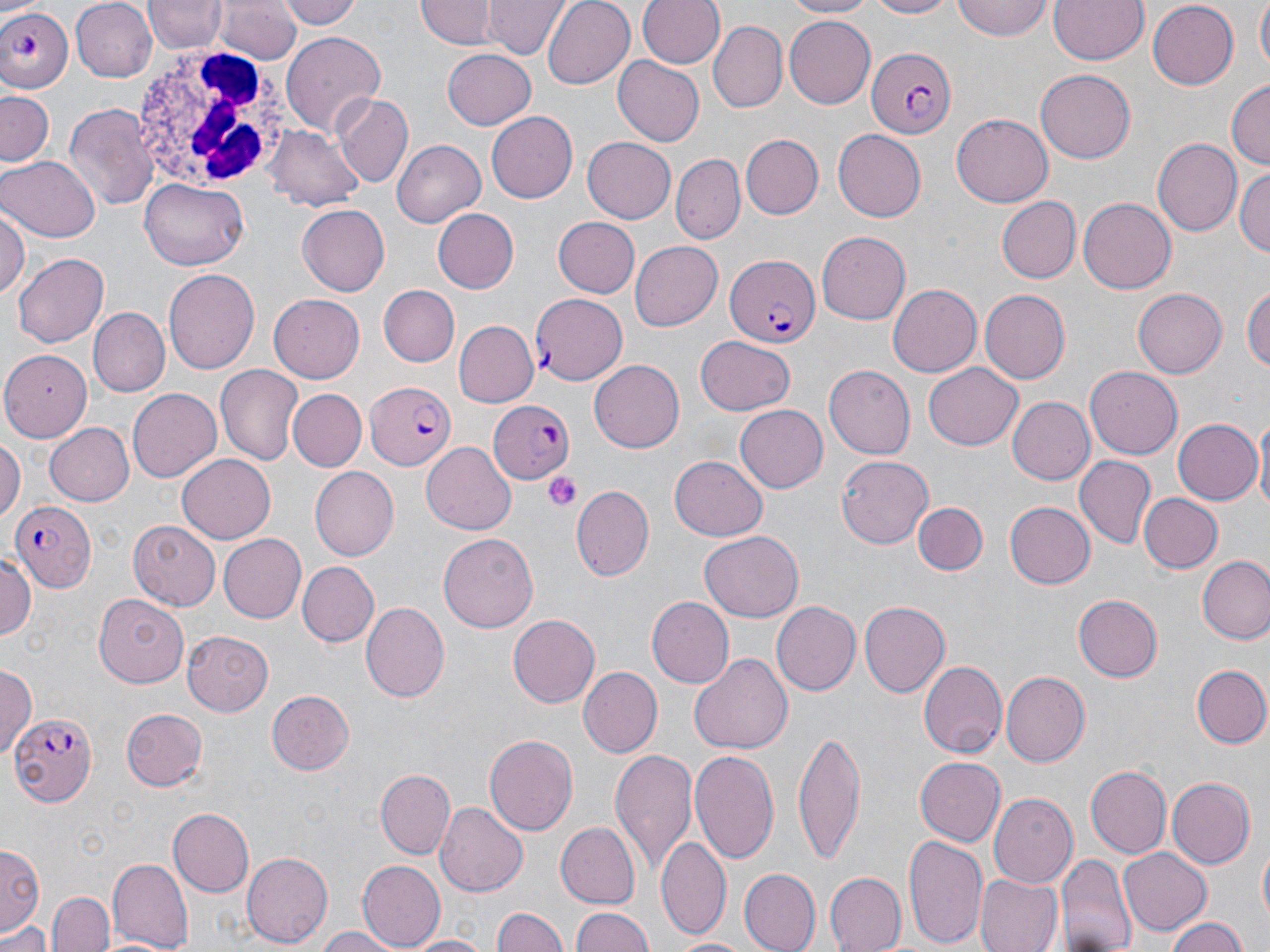

Summary:
  - Coordinate format: approximate bounding boxes as named x1/y1/x2/y2 corners in pixels
  - White blood cell locations: (x1=132, y1=45, x2=301, y2=196)
  - Plasmodium falciparum-infected red blood cell locations: (x1=2, y1=3, x2=75, y2=92), (x1=867, y1=48, x2=956, y2=139), (x1=724, y1=253, x2=817, y2=346), (x1=529, y1=293, x2=629, y2=386), (x1=364, y1=383, x2=453, y2=470), (x1=486, y1=399, x2=575, y2=481), (x1=14, y1=499, x2=96, y2=591), (x1=9, y1=710, x2=96, y2=808)
  - Platelet locations: (x1=543, y1=469, x2=584, y2=511)
  - Uninfected red blood cell locations: (x1=146, y1=0, x2=225, y2=54), (x1=281, y1=0, x2=362, y2=32), (x1=418, y1=0, x2=496, y2=50), (x1=486, y1=0, x2=567, y2=60), (x1=542, y1=0, x2=635, y2=89), (x1=638, y1=0, x2=724, y2=69), (x1=780, y1=0, x2=882, y2=18), (x1=860, y1=0, x2=961, y2=19), (x1=953, y1=0, x2=1052, y2=41), (x1=1049, y1=0, x2=1147, y2=65), (x1=1254, y1=0, x2=1270, y2=71), (x1=73, y1=1, x2=157, y2=82), (x1=217, y1=1, x2=301, y2=65), (x1=1146, y1=3, x2=1240, y2=88), (x1=785, y1=16, x2=875, y2=108), (x1=709, y1=22, x2=786, y2=110), (x1=281, y1=31, x2=386, y2=139), (x1=441, y1=48, x2=537, y2=129), (x1=612, y1=57, x2=704, y2=148), (x1=1036, y1=69, x2=1135, y2=162), (x1=1227, y1=79, x2=1270, y2=173), (x1=1, y1=89, x2=55, y2=167), (x1=334, y1=93, x2=413, y2=187), (x1=63, y1=103, x2=160, y2=211), (x1=485, y1=108, x2=577, y2=200), (x1=951, y1=115, x2=1054, y2=206), (x1=266, y1=126, x2=366, y2=210), (x1=833, y1=128, x2=926, y2=219), (x1=741, y1=134, x2=823, y2=219), (x1=582, y1=136, x2=676, y2=222), (x1=390, y1=138, x2=484, y2=227), (x1=1153, y1=138, x2=1241, y2=238), (x1=672, y1=154, x2=744, y2=241), (x1=0, y1=155, x2=99, y2=242), (x1=1233, y1=167, x2=1269, y2=256), (x1=140, y1=177, x2=251, y2=269), (x1=995, y1=195, x2=1081, y2=283), (x1=1079, y1=196, x2=1177, y2=294), (x1=296, y1=205, x2=390, y2=296), (x1=0, y1=209, x2=29, y2=301), (x1=432, y1=209, x2=519, y2=293), (x1=552, y1=217, x2=639, y2=298), (x1=818, y1=231, x2=910, y2=324), (x1=631, y1=240, x2=723, y2=329), (x1=13, y1=253, x2=109, y2=347), (x1=164, y1=269, x2=260, y2=374), (x1=1243, y1=282, x2=1270, y2=379), (x1=377, y1=284, x2=460, y2=366), (x1=886, y1=285, x2=980, y2=378), (x1=1133, y1=286, x2=1227, y2=375), (x1=978, y1=290, x2=1069, y2=384), (x1=268, y1=294, x2=365, y2=383), (x1=90, y1=308, x2=168, y2=396), (x1=453, y1=321, x2=539, y2=408), (x1=697, y1=334, x2=795, y2=415), (x1=0, y1=350, x2=92, y2=441), (x1=590, y1=359, x2=689, y2=452), (x1=924, y1=362, x2=1024, y2=450), (x1=1086, y1=364, x2=1183, y2=456), (x1=215, y1=365, x2=303, y2=465), (x1=824, y1=365, x2=915, y2=459), (x1=126, y1=388, x2=219, y2=482), (x1=287, y1=388, x2=366, y2=471), (x1=1006, y1=396, x2=1095, y2=485), (x1=737, y1=407, x2=827, y2=491), (x1=1254, y1=417, x2=1270, y2=518), (x1=1171, y1=418, x2=1260, y2=505), (x1=45, y1=422, x2=134, y2=506), (x1=0, y1=437, x2=23, y2=524), (x1=421, y1=442, x2=516, y2=535), (x1=177, y1=454, x2=275, y2=542), (x1=834, y1=455, x2=933, y2=548), (x1=1076, y1=455, x2=1154, y2=547), (x1=670, y1=456, x2=769, y2=541), (x1=310, y1=467, x2=400, y2=559), (x1=570, y1=485, x2=654, y2=582), (x1=1138, y1=493, x2=1222, y2=573), (x1=1004, y1=501, x2=1095, y2=589), (x1=912, y1=502, x2=988, y2=576), (x1=131, y1=519, x2=220, y2=611), (x1=438, y1=532, x2=537, y2=634), (x1=699, y1=532, x2=803, y2=621), (x1=217, y1=533, x2=307, y2=623), (x1=0, y1=552, x2=36, y2=647), (x1=1197, y1=555, x2=1270, y2=645), (x1=299, y1=561, x2=379, y2=646), (x1=94, y1=591, x2=191, y2=686), (x1=1074, y1=594, x2=1163, y2=681), (x1=645, y1=596, x2=734, y2=689), (x1=771, y1=600, x2=861, y2=696), (x1=859, y1=601, x2=950, y2=695), (x1=360, y1=602, x2=449, y2=703), (x1=508, y1=614, x2=599, y2=708), (x1=182, y1=632, x2=274, y2=716), (x1=688, y1=651, x2=793, y2=754), (x1=917, y1=660, x2=1005, y2=758), (x1=1, y1=663, x2=36, y2=759), (x1=1190, y1=664, x2=1269, y2=747), (x1=579, y1=667, x2=661, y2=755), (x1=1001, y1=671, x2=1090, y2=767), (x1=266, y1=691, x2=354, y2=774), (x1=120, y1=709, x2=208, y2=791), (x1=792, y1=731, x2=868, y2=864), (x1=484, y1=732, x2=578, y2=838), (x1=690, y1=747, x2=782, y2=867), (x1=610, y1=748, x2=697, y2=872), (x1=914, y1=756, x2=1006, y2=847), (x1=1085, y1=765, x2=1170, y2=856), (x1=377, y1=767, x2=453, y2=859), (x1=1168, y1=777, x2=1255, y2=869), (x1=989, y1=793, x2=1077, y2=890), (x1=435, y1=801, x2=527, y2=898), (x1=168, y1=807, x2=253, y2=896), (x1=554, y1=822, x2=640, y2=909), (x1=903, y1=833, x2=989, y2=951), (x1=655, y1=835, x2=731, y2=939), (x1=1257, y1=839, x2=1269, y2=934), (x1=1, y1=844, x2=43, y2=934), (x1=1119, y1=847, x2=1213, y2=934), (x1=241, y1=850, x2=334, y2=947), (x1=1055, y1=854, x2=1137, y2=952), (x1=107, y1=857, x2=193, y2=951), (x1=359, y1=860, x2=444, y2=949), (x1=741, y1=869, x2=820, y2=952), (x1=823, y1=873, x2=905, y2=952), (x1=975, y1=873, x2=1063, y2=952), (x1=50, y1=891, x2=115, y2=952), (x1=492, y1=906, x2=567, y2=952), (x1=568, y1=906, x2=658, y2=951), (x1=1166, y1=916, x2=1248, y2=952), (x1=0, y1=918, x2=53, y2=952), (x1=309, y1=925, x2=407, y2=952), (x1=403, y1=933, x2=489, y2=952), (x1=666, y1=935, x2=754, y2=951)
  - Slide-level diagnosis: Plasmodium falciparum
  - Magnification: 1000x
  - Field of view: single
  - Modality: light microscopy
  - Stain: May-Grünwald-Giemsa
  - Image size: 1270×952 pixels
  - Preparation: thin blood film